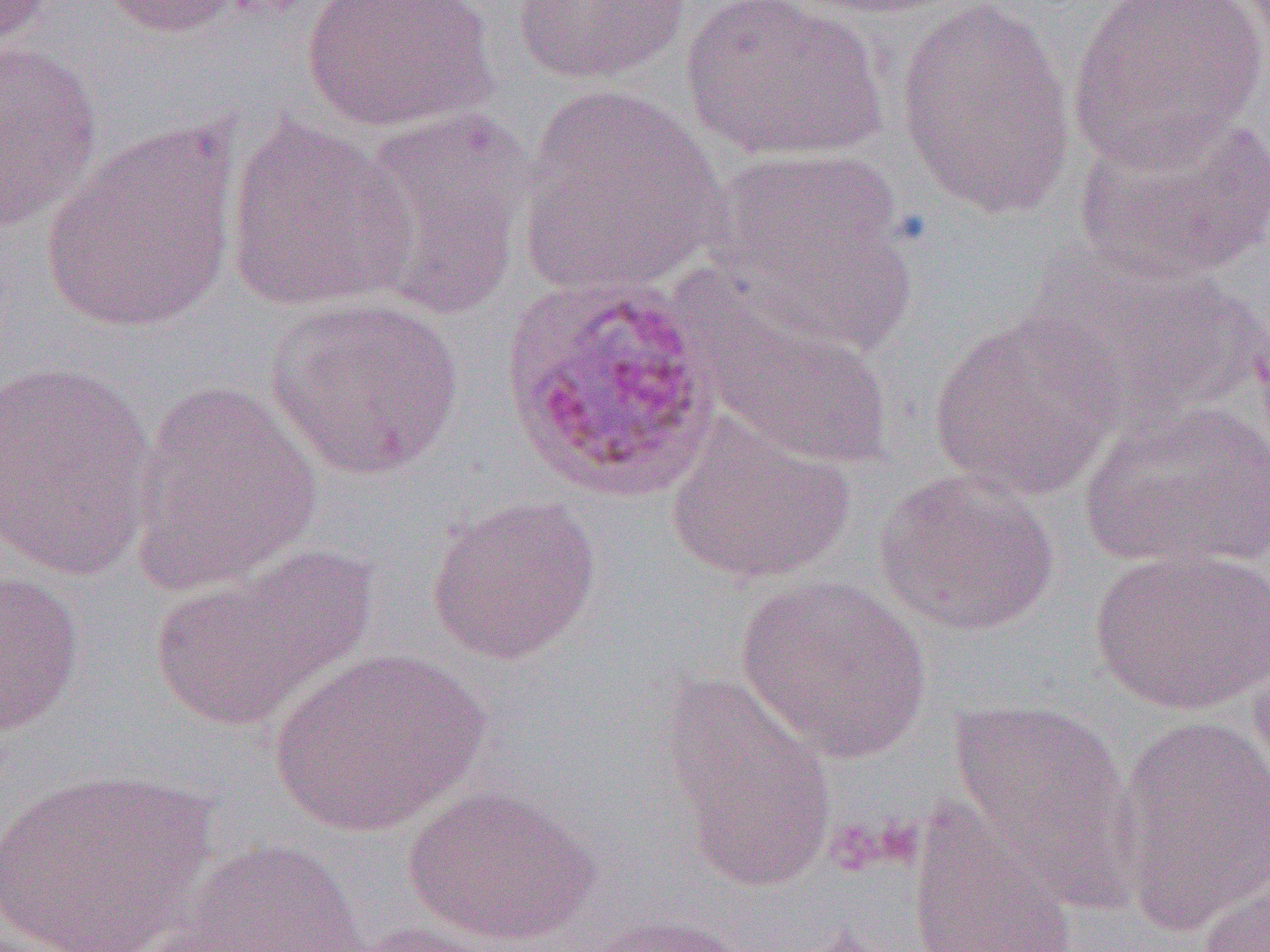

Approximate bounding boxes as (x1, y1, x2, y2) in pixels. Uninfected red blood cell locations: (1, 0, 57, 50), (98, 0, 251, 37), (301, 0, 499, 134), (512, 0, 691, 85), (681, 0, 886, 163), (793, 0, 971, 18), (894, 0, 1079, 221), (1067, 0, 1267, 171), (0, 40, 104, 233), (517, 84, 724, 298), (347, 106, 535, 319), (1073, 109, 1269, 286), (222, 117, 420, 315), (39, 121, 240, 333), (702, 149, 914, 342), (1025, 248, 1252, 430), (264, 295, 465, 481), (689, 295, 896, 471), (928, 310, 1125, 502), (0, 361, 159, 581), (128, 380, 325, 597), (1079, 399, 1270, 573), (664, 415, 855, 586), (873, 468, 1061, 637), (425, 494, 601, 665), (1090, 545, 1270, 716), (149, 547, 377, 732), (0, 569, 86, 735), (736, 575, 932, 763), (1245, 629, 1270, 797), (271, 649, 488, 837), (658, 672, 836, 891), (948, 698, 1139, 895), (1110, 714, 1270, 937), (0, 766, 217, 951), (402, 782, 601, 947), (906, 798, 1081, 952), (165, 839, 368, 952), (1191, 875, 1269, 950), (582, 913, 754, 952), (344, 921, 512, 952). Slide-level diagnosis: Plasmodium ovale. Thin blood smear. 1000x magnification. Image is 1270×952 pixels. Optical microscopy. One field of a larger specimen.